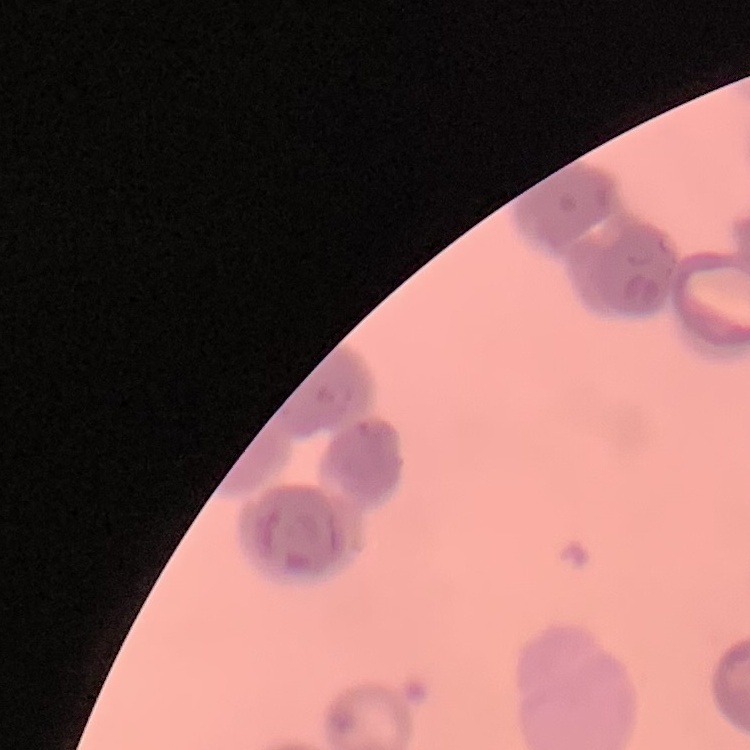 The erythrocytes exhibit rouleaux formation. Square crop of a larger photomicrograph. Thin blood film. Stained with either Field's or Giemsa.